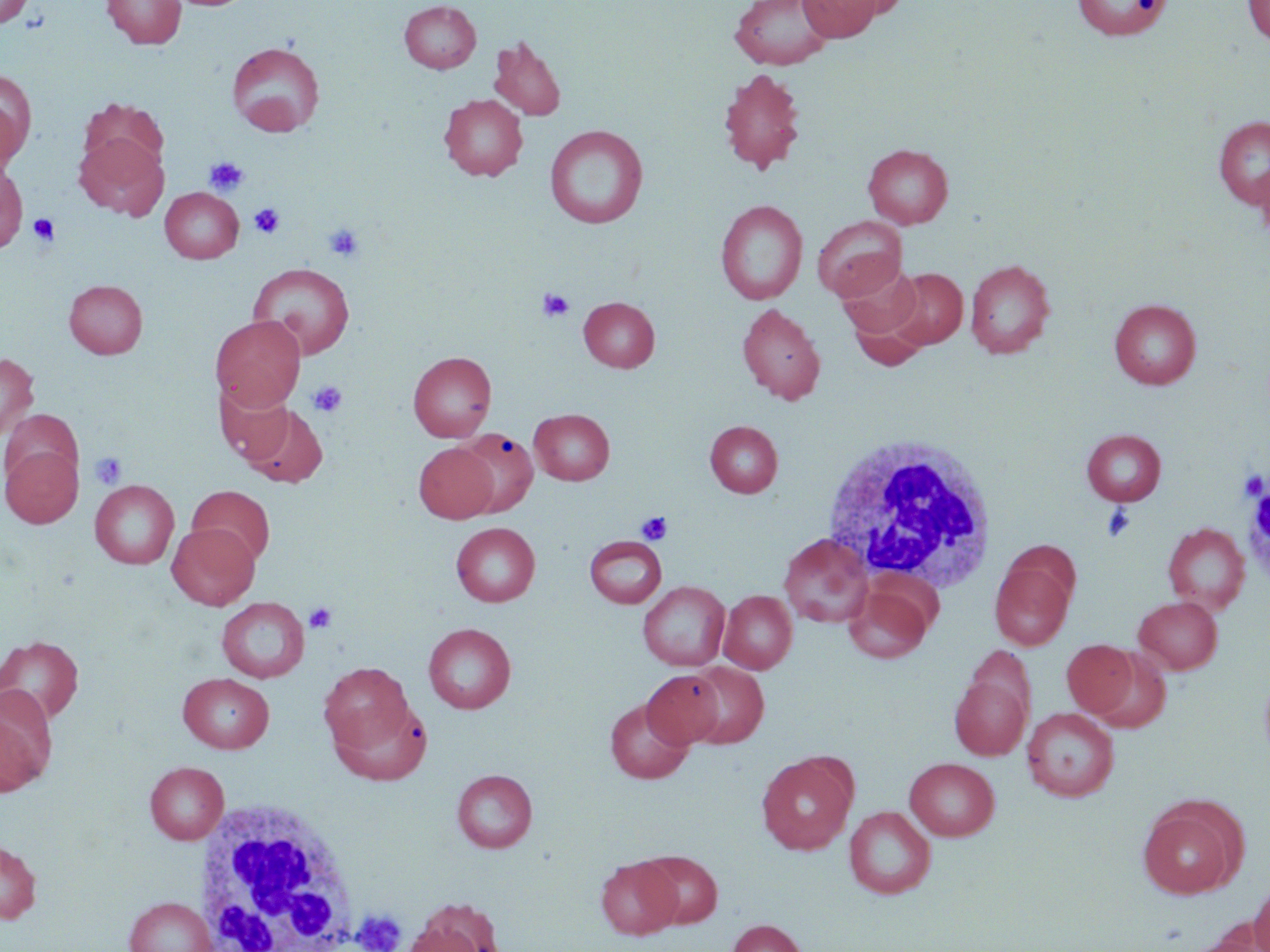

slide-level diagnosis = no evidence of blood parasites
preparation = thin blood film
stain = May-Grünwald-Giemsa
platelet locations = approximate bounding boxes as named x1/y1/x2/y2 corners in pixels: (x1=204, y1=156, x2=249, y2=195), (x1=249, y1=202, x2=286, y2=238), (x1=28, y1=213, x2=60, y2=246), (x1=323, y1=222, x2=364, y2=262), (x1=538, y1=287, x2=574, y2=322), (x1=307, y1=380, x2=348, y2=419), (x1=90, y1=451, x2=127, y2=489), (x1=1239, y1=470, x2=1269, y2=501), (x1=1101, y1=504, x2=1137, y2=542), (x1=635, y1=511, x2=671, y2=545), (x1=304, y1=603, x2=337, y2=633), (x1=352, y1=909, x2=407, y2=952)
image size = 1270×952 pixels
magnification = 1000x
uninfected red blood cell locations = approximate bounding boxes as named x1/y1/x2/y2 corners in pixels: (x1=0, y1=0, x2=33, y2=27), (x1=102, y1=0, x2=186, y2=49), (x1=797, y1=0, x2=882, y2=41), (x1=831, y1=0, x2=911, y2=20), (x1=1072, y1=0, x2=1172, y2=40), (x1=1242, y1=0, x2=1270, y2=47), (x1=398, y1=1, x2=481, y2=73), (x1=729, y1=1, x2=835, y2=70), (x1=489, y1=35, x2=567, y2=122), (x1=227, y1=41, x2=325, y2=136), (x1=718, y1=68, x2=806, y2=174), (x1=0, y1=70, x2=34, y2=166), (x1=439, y1=94, x2=527, y2=181), (x1=78, y1=98, x2=168, y2=179), (x1=1213, y1=117, x2=1270, y2=210), (x1=545, y1=125, x2=648, y2=228), (x1=75, y1=132, x2=167, y2=220), (x1=863, y1=143, x2=953, y2=228), (x1=1255, y1=159, x2=1270, y2=243), (x1=0, y1=161, x2=28, y2=253), (x1=159, y1=187, x2=243, y2=263), (x1=716, y1=200, x2=808, y2=305), (x1=812, y1=215, x2=907, y2=300), (x1=965, y1=259, x2=1056, y2=358), (x1=837, y1=262, x2=923, y2=340), (x1=248, y1=263, x2=355, y2=359), (x1=888, y1=268, x2=967, y2=349), (x1=64, y1=279, x2=147, y2=359), (x1=579, y1=297, x2=660, y2=372), (x1=1110, y1=299, x2=1201, y2=389), (x1=737, y1=303, x2=825, y2=404), (x1=848, y1=306, x2=929, y2=371), (x1=210, y1=315, x2=305, y2=411), (x1=408, y1=351, x2=497, y2=441), (x1=0, y1=352, x2=39, y2=441), (x1=215, y1=382, x2=297, y2=464), (x1=236, y1=401, x2=329, y2=488), (x1=1, y1=407, x2=83, y2=495), (x1=529, y1=409, x2=615, y2=485), (x1=705, y1=421, x2=783, y2=497), (x1=456, y1=427, x2=538, y2=517), (x1=1082, y1=429, x2=1166, y2=506), (x1=1, y1=442, x2=83, y2=528), (x1=414, y1=443, x2=498, y2=522), (x1=90, y1=480, x2=179, y2=569), (x1=187, y1=486, x2=275, y2=567), (x1=167, y1=522, x2=259, y2=610), (x1=451, y1=522, x2=540, y2=606), (x1=1163, y1=522, x2=1250, y2=613), (x1=779, y1=533, x2=874, y2=628), (x1=584, y1=535, x2=667, y2=608), (x1=990, y1=558, x2=1075, y2=650), (x1=638, y1=581, x2=730, y2=670), (x1=844, y1=583, x2=933, y2=663), (x1=719, y1=590, x2=797, y2=674), (x1=1134, y1=596, x2=1223, y2=674), (x1=217, y1=598, x2=309, y2=683), (x1=423, y1=623, x2=516, y2=713), (x1=0, y1=635, x2=84, y2=724), (x1=1062, y1=640, x2=1138, y2=717), (x1=1089, y1=650, x2=1172, y2=732), (x1=319, y1=662, x2=415, y2=759), (x1=685, y1=662, x2=768, y2=748), (x1=1259, y1=667, x2=1270, y2=771), (x1=643, y1=670, x2=724, y2=747), (x1=178, y1=673, x2=274, y2=753), (x1=950, y1=674, x2=1031, y2=760), (x1=0, y1=693, x2=54, y2=798), (x1=605, y1=698, x2=694, y2=784), (x1=332, y1=705, x2=440, y2=786), (x1=1022, y1=707, x2=1119, y2=802), (x1=757, y1=753, x2=855, y2=855), (x1=905, y1=757, x2=999, y2=841), (x1=145, y1=762, x2=229, y2=844), (x1=452, y1=769, x2=537, y2=853), (x1=1137, y1=800, x2=1242, y2=899), (x1=845, y1=806, x2=935, y2=899), (x1=0, y1=839, x2=41, y2=925), (x1=638, y1=850, x2=723, y2=929), (x1=596, y1=857, x2=681, y2=939), (x1=1250, y1=878, x2=1270, y2=952), (x1=125, y1=897, x2=217, y2=952), (x1=406, y1=898, x2=504, y2=952), (x1=727, y1=919, x2=808, y2=952), (x1=1183, y1=927, x2=1268, y2=952)
modality = light microscopy
white blood cell locations = approximate bounding boxes as named x1/y1/x2/y2 corners in pixels: (x1=820, y1=433, x2=998, y2=590), (x1=193, y1=798, x2=358, y2=949)
field of view = single